Report the malaria status of this cell.
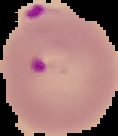
It is parasitized.

image type = segmented cell region on a black background
preparation = thin blood film
image size = 118×136 pixels